Comment on the morphology of the erythrocytes.
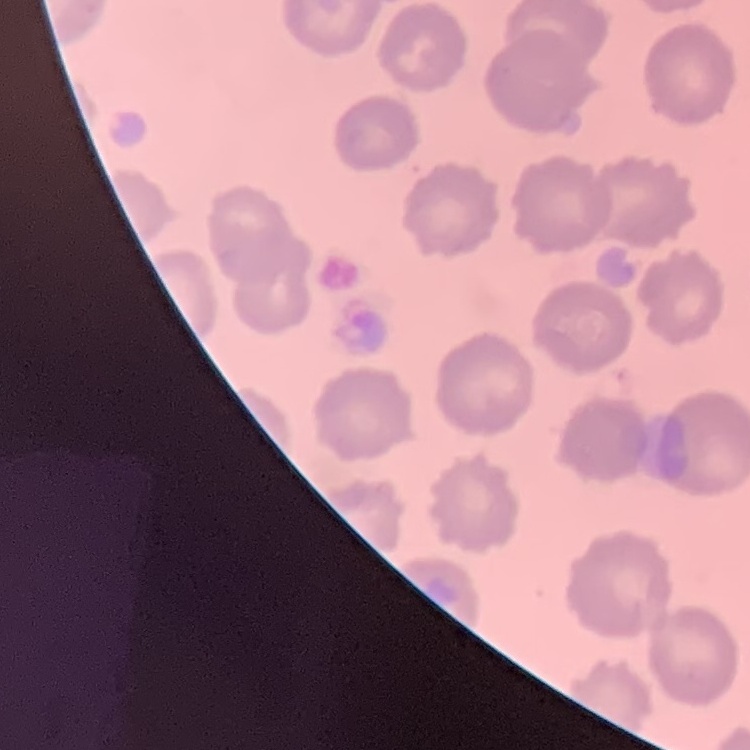

No rouleaux formation.

preparation = thin blood film
stain = Field's or Giemsa
image type = square crop of a larger photomicrograph